Identify the cell.
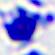
This is a leukocyte.

Summary:
  - Magnification: 400x
  - Modality: micrograph